Point out each malaria parasite and classify it by life-cycle stage.
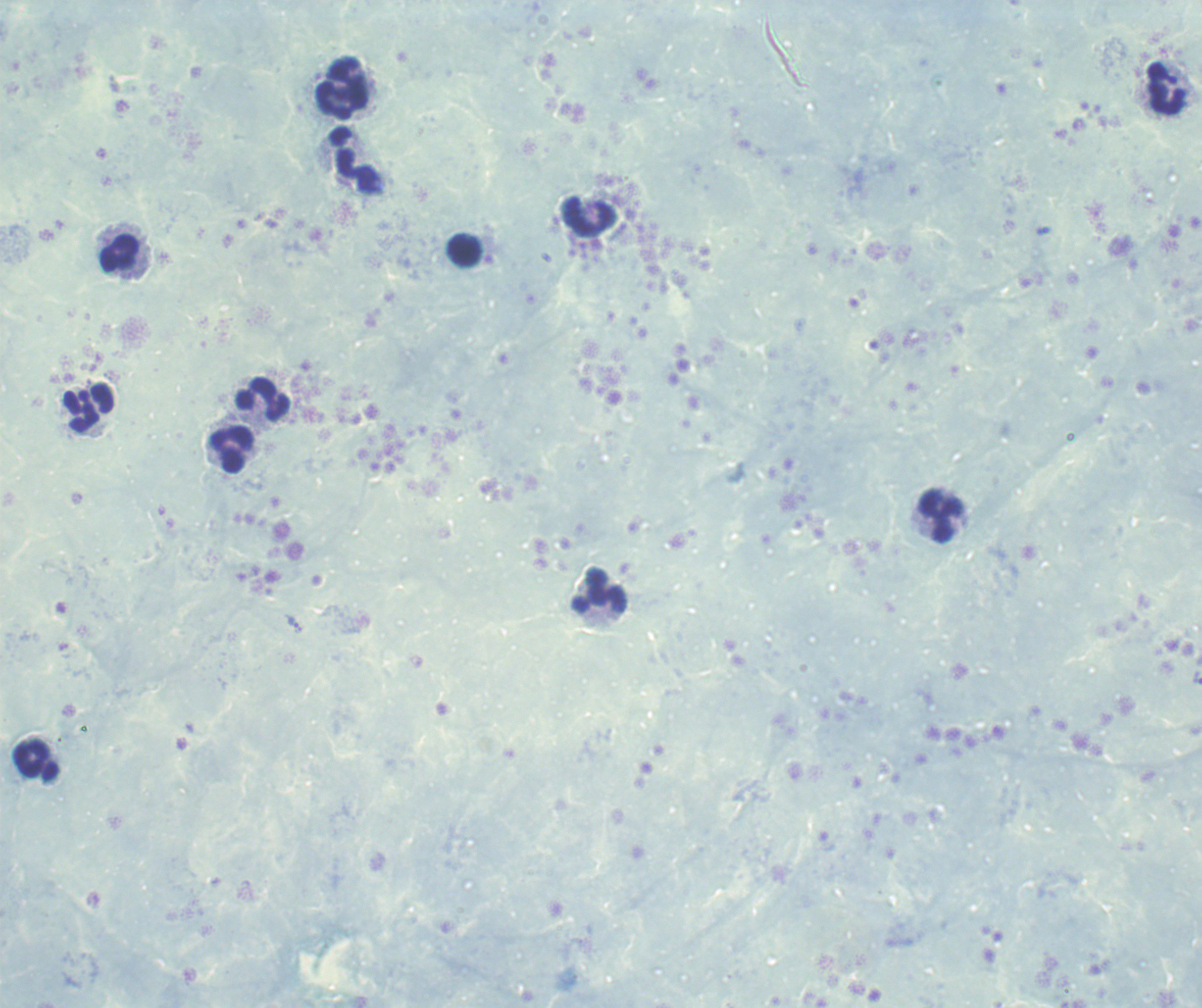
No malaria parasites seen.

Approximate object centers, in pixels from the top-left corner.
Summary:
  - Leukocyte locations: (x=1167, y=88), (x=344, y=89), (x=357, y=162), (x=589, y=217), (x=464, y=250), (x=120, y=253), (x=264, y=399), (x=89, y=409), (x=231, y=451), (x=940, y=518), (x=599, y=590), (x=36, y=760)
  - Context: previously used in an actual diagnosis
  - Field of view: one from this slide
  - Background quality: unsatisfactory
  - Image size: 1202×1008 pixels
  - Preparation: thick blood smear
  - Magnification: 100x
  - Stain: Romanowsky